Locate every blood parasite and identify its species.
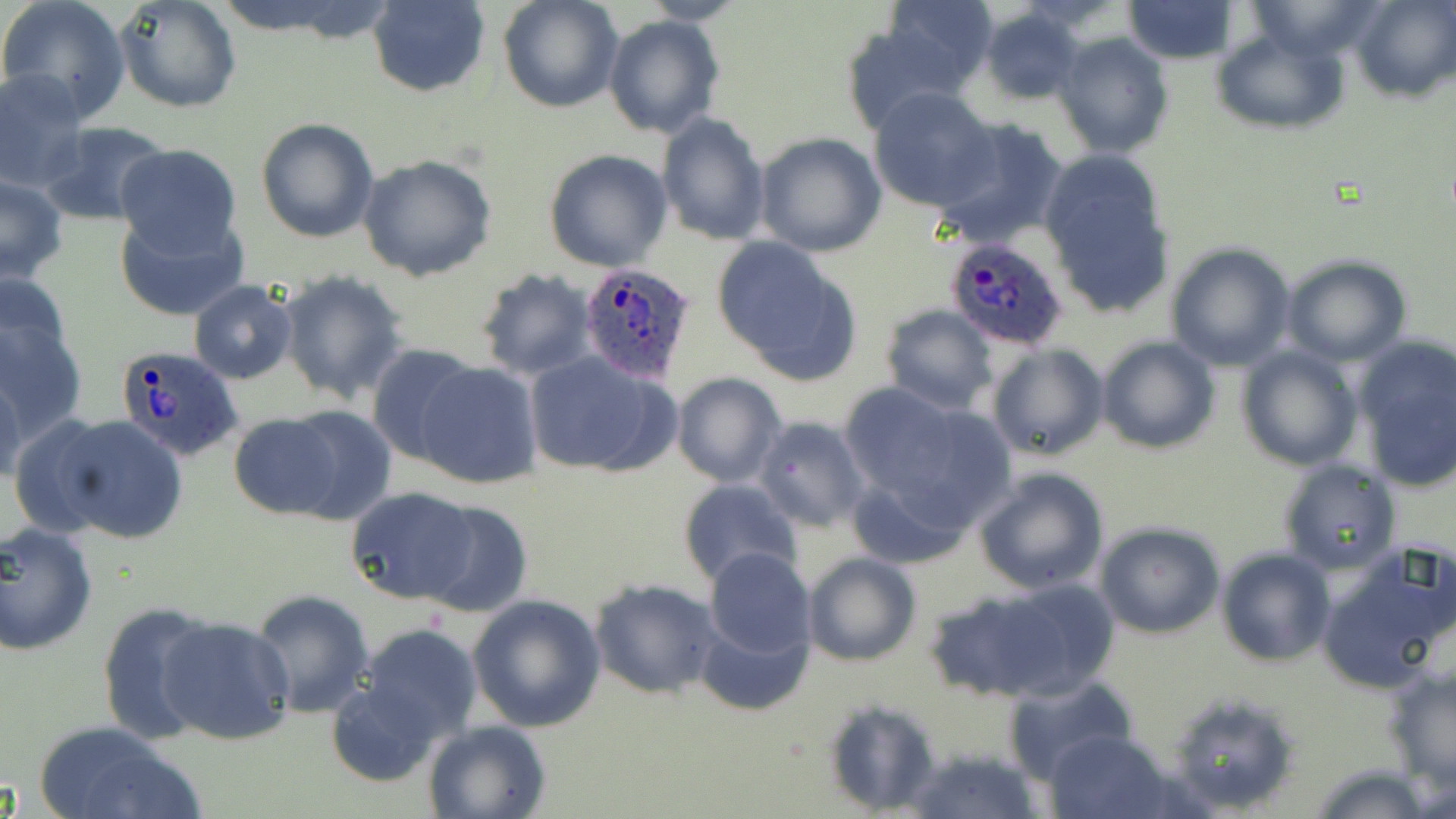
Approximate bounding boxes as [x1, y1, x2, y2] in pixels.
Plasmodium ovale-infected red blood cells: [941, 232, 1069, 351], [576, 261, 700, 386], [112, 344, 245, 462].
No Plasmodium falciparum, Plasmodium malariae, Plasmodium vivax, Babesia divergens, or Trypanosoma brucei observed.

Uninfected red blood cell locations: [0, 0, 131, 122], [114, 0, 243, 115], [365, 0, 491, 98], [498, 0, 623, 113], [639, 0, 752, 24], [881, 0, 998, 97], [1121, 0, 1243, 64], [1244, 0, 1389, 64], [1350, 0, 1454, 102], [979, 6, 1085, 106], [602, 15, 724, 138], [839, 18, 970, 136], [1211, 29, 1350, 133], [1052, 33, 1174, 160], [0, 69, 88, 192], [869, 87, 998, 212], [656, 112, 771, 246], [936, 116, 1070, 249], [254, 117, 379, 243], [38, 122, 173, 226], [753, 131, 886, 257], [112, 144, 245, 260], [543, 150, 673, 272], [1039, 152, 1174, 318], [357, 154, 498, 282], [0, 177, 70, 285], [113, 207, 245, 323], [712, 237, 860, 385], [1165, 243, 1294, 370], [1282, 255, 1413, 367], [1, 267, 73, 380], [475, 270, 598, 380], [277, 271, 410, 404], [188, 280, 298, 383], [881, 305, 998, 415], [0, 315, 88, 445], [1349, 333, 1456, 491], [1097, 336, 1222, 455], [364, 343, 481, 467], [984, 343, 1109, 463], [1236, 344, 1363, 472], [524, 350, 674, 478], [414, 361, 544, 490], [0, 363, 25, 489], [670, 372, 787, 488], [836, 384, 1012, 542], [282, 406, 399, 524], [227, 413, 342, 518], [34, 414, 189, 544], [753, 416, 869, 532], [1276, 459, 1401, 576], [975, 467, 1110, 597], [677, 479, 801, 591], [346, 488, 480, 604], [417, 499, 533, 617], [0, 522, 99, 656], [1093, 523, 1226, 640], [1216, 547, 1336, 665], [1321, 547, 1456, 690], [702, 548, 816, 662], [803, 551, 922, 668], [608, 567, 819, 676], [589, 577, 726, 701], [962, 578, 1123, 703], [249, 589, 378, 718], [466, 593, 607, 732], [96, 603, 219, 744], [696, 608, 813, 719], [155, 614, 296, 746], [359, 623, 483, 743], [1383, 665, 1456, 789], [1002, 674, 1138, 787], [324, 683, 443, 785], [1160, 691, 1298, 814], [820, 696, 943, 814], [32, 719, 201, 819], [424, 719, 551, 819], [1046, 728, 1174, 818], [904, 746, 1039, 819], [1308, 765, 1441, 819]. Slide-level diagnosis: Plasmodium ovale. Light microscopy. May-Grünwald-Giemsa-stained preparation. Thin blood smear. 1000x magnification. Image is 1456×819 pixels. One field of a larger specimen.